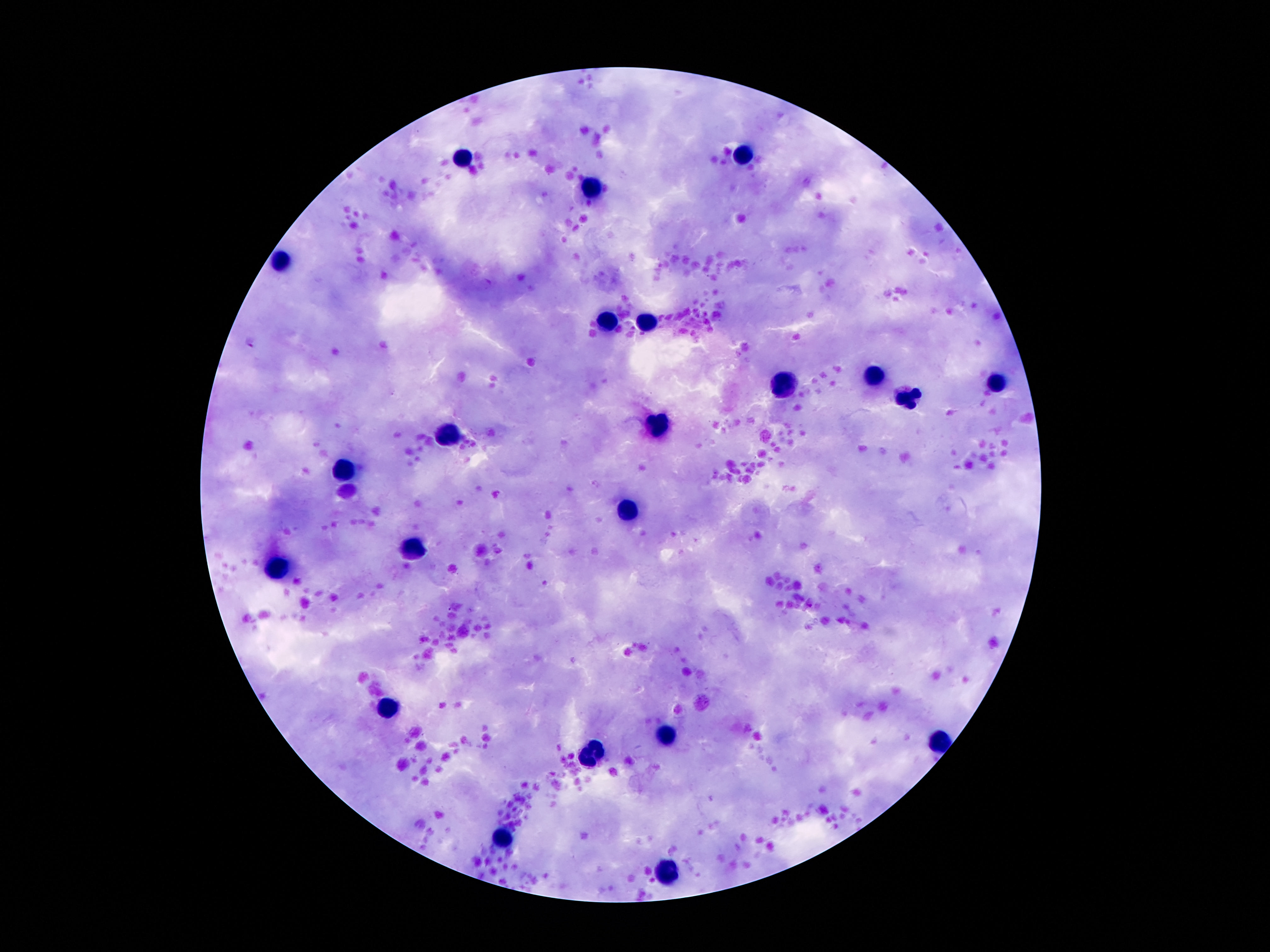

Approximate centers as (x, y) in pixels.
Summary:
  - Leukocyte locations: (746, 152), (462, 155), (595, 187), (282, 260), (607, 320), (648, 320), (872, 379), (996, 383), (786, 386), (909, 399), (660, 425), (450, 434), (348, 468), (627, 511), (415, 549), (277, 565), (389, 706), (665, 736), (937, 740), (590, 753), (502, 839), (667, 872)
  - Field of view: one from this slide
  - Magnification: 100x
  - Stain: Giemsa
  - Preparation: thick blood smear
  - Patient malaria status: not infected
  - Image size: 1270×952 pixels
  - Capture: smartphone camera through the microscope eyepiece